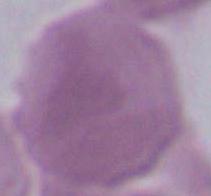 An erythrocyte is seen. 1000x magnification. Micrograph.